Name the parasite shown.
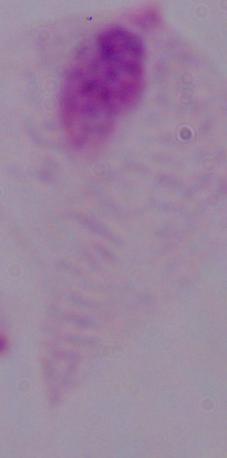

A trichomonad.

Summary:
  - Magnification: 1000x
  - Modality: micrograph